Identify the blood parasite species.
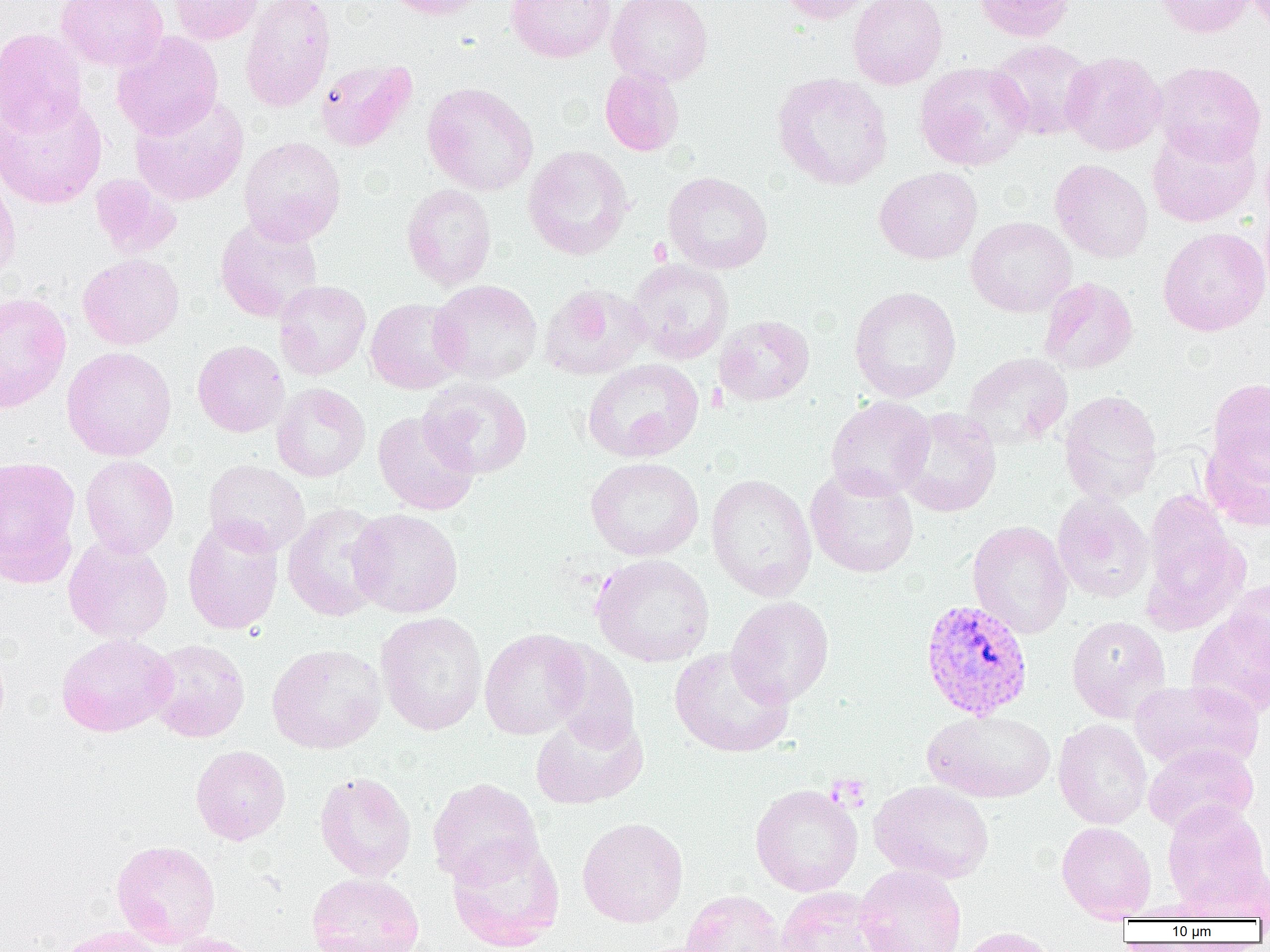
Plasmodium vivax.

uninfected red blood cell locations = approximate bounding boxes as (x1, y1, x2, y2) in pixels: (55, 0, 168, 71), (169, 0, 264, 45), (240, 0, 336, 113), (383, 0, 492, 19), (505, 0, 615, 63), (608, 0, 713, 87), (778, 0, 874, 23), (848, 0, 948, 90), (972, 0, 1076, 42), (1155, 0, 1257, 38), (0, 27, 88, 135), (112, 32, 223, 140), (987, 38, 1097, 140), (1061, 51, 1167, 156), (315, 58, 417, 152), (1153, 61, 1266, 166), (914, 62, 1033, 170), (599, 66, 685, 156), (771, 72, 893, 190), (422, 82, 538, 196), (0, 93, 107, 209), (130, 95, 249, 205), (1147, 125, 1260, 227), (238, 136, 346, 245), (523, 145, 633, 260), (1050, 159, 1153, 263), (874, 166, 982, 264), (0, 171, 20, 287), (662, 171, 773, 274), (90, 174, 181, 258), (401, 184, 497, 290), (215, 215, 323, 323), (966, 216, 1076, 317), (1158, 227, 1269, 336), (77, 253, 184, 350), (627, 258, 734, 364), (1038, 277, 1138, 375), (274, 280, 371, 381), (428, 280, 543, 383), (540, 284, 650, 380), (849, 286, 962, 403), (0, 292, 72, 413), (365, 298, 466, 394), (714, 315, 814, 406), (192, 340, 289, 437), (61, 347, 177, 461), (961, 352, 1073, 451), (582, 358, 704, 462), (419, 377, 533, 479), (1207, 378, 1270, 481), (271, 383, 370, 482), (1059, 390, 1162, 505), (825, 396, 935, 501), (895, 407, 1001, 518), (373, 410, 479, 516), (1201, 430, 1270, 531), (80, 455, 179, 558), (0, 456, 81, 586), (585, 457, 704, 561), (203, 459, 310, 557), (805, 467, 919, 578), (706, 474, 817, 601), (1142, 492, 1249, 634), (1052, 493, 1154, 604), (282, 503, 389, 622), (348, 508, 464, 618), (182, 517, 283, 635), (967, 521, 1073, 638), (64, 537, 173, 643), (591, 554, 714, 667), (1225, 579, 1270, 672), (726, 595, 834, 707), (1186, 610, 1270, 718), (375, 611, 487, 736), (1067, 615, 1171, 722), (479, 628, 590, 739), (56, 632, 177, 737), (146, 639, 250, 742), (547, 642, 640, 752), (266, 643, 387, 754), (669, 646, 794, 758), (1130, 679, 1264, 772), (922, 709, 1055, 803), (530, 711, 648, 809), (1053, 718, 1152, 829), (1143, 743, 1259, 835), (191, 745, 291, 845), (314, 771, 416, 881), (427, 777, 543, 886), (868, 780, 994, 884), (750, 784, 863, 896), (1162, 801, 1268, 910), (577, 817, 688, 928), (1056, 821, 1156, 922), (446, 835, 566, 951), (111, 839, 221, 948), (855, 864, 967, 952), (1183, 864, 1270, 921), (306, 872, 425, 952), (775, 887, 891, 952), (680, 890, 788, 952), (1120, 903, 1219, 922), (53, 926, 166, 952), (957, 926, 1059, 952), (164, 932, 261, 952)
modality = light microscopy
Plasmodium vivax-infected red blood cell locations = approximate bounding boxes as (x1, y1, x2, y2) in pixels: (920, 599, 1034, 720)
preparation = thin blood film
magnification = 1000x
field of view = single
image size = 1270×952 pixels